Report the malaria status of this cell.
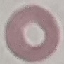

Uninfected.

Summary:
  - Image type: automatically extracted cell patch, resized to 64 × 64 pixels
  - Stain: Giemsa
  - Capture: smartphone camera at the microscope eyepiece
  - Preparation: thin blood film